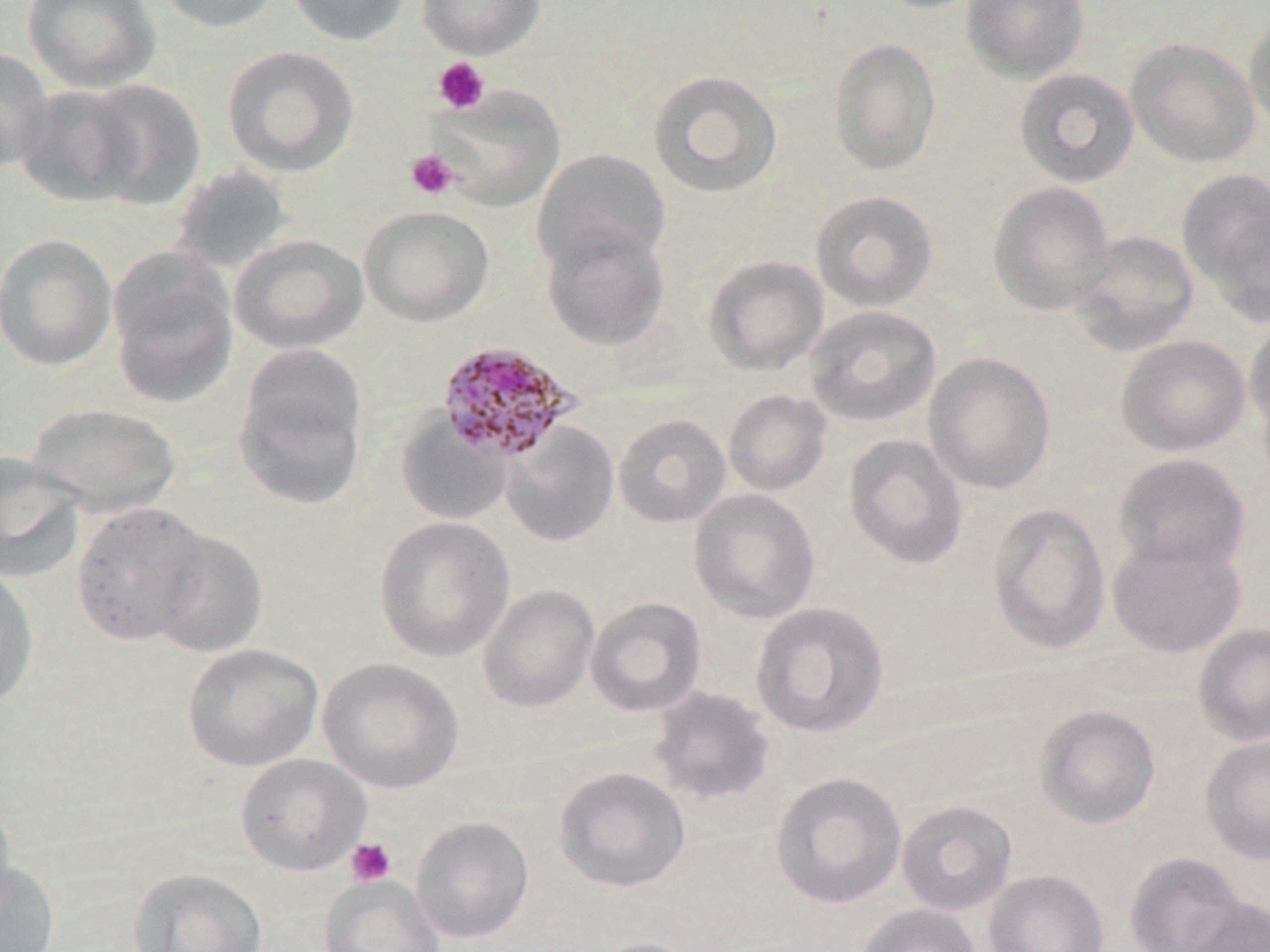

Approximate bounding boxes as (x1,y1)-(x2,y2) corner pairs in pixels. Platelet locations: (432,57)-(490,114), (405,149)-(458,200), (345,837)-(397,886). Plasmodium malariae-infected red blood cell locations: (435,341)-(579,463). Uninfected red blood cell locations: (22,0)-(161,93), (154,0)-(284,34), (286,0)-(410,46), (417,0)-(546,58), (871,0)-(984,14), (962,0)-(1090,84), (1244,9)-(1270,136), (828,37)-(941,176), (1125,37)-(1261,169), (222,45)-(359,176), (0,48)-(55,171), (1014,67)-(1140,187), (647,69)-(783,199), (81,79)-(206,210), (12,84)-(147,208), (429,84)-(566,212), (532,148)-(672,274), (168,164)-(293,276), (1177,168)-(1270,321), (987,181)-(1116,315), (810,190)-(939,312), (359,204)-(494,327), (540,222)-(671,350), (1068,231)-(1199,355), (0,233)-(117,371), (229,234)-(368,353), (106,247)-(240,410), (703,255)-(829,375), (804,305)-(942,427), (1244,315)-(1270,440), (1115,334)-(1251,457), (232,347)-(369,511), (924,351)-(1056,495), (723,389)-(831,496), (25,402)-(183,519), (394,412)-(514,526), (613,413)-(732,529), (501,420)-(620,547), (844,434)-(969,571), (0,452)-(87,584), (1113,452)-(1252,575), (688,488)-(821,624), (71,501)-(212,646), (986,502)-(1111,654), (374,516)-(515,662), (147,528)-(269,660), (1107,533)-(1246,658), (0,565)-(39,709), (477,585)-(600,713), (585,596)-(708,717), (750,601)-(890,739), (1193,623)-(1270,746), (181,643)-(325,772), (317,657)-(464,794), (649,686)-(777,808), (1035,704)-(1161,829), (1199,734)-(1270,865), (235,754)-(371,876), (553,766)-(691,893), (770,771)-(907,909), (0,795)-(16,922), (897,800)-(1018,916), (410,815)-(535,944), (1124,852)-(1247,952), (0,858)-(61,952), (126,867)-(269,952), (983,869)-(1110,952), (318,874)-(445,952), (1181,895)-(1270,952), (856,904)-(980,952), (586,937)-(706,952). Slide-level diagnosis: Plasmodium malariae. One field of a larger specimen. Captured at 1000x magnification. May-Grünwald-Giemsa stain. Thin blood film. Image is 1270×952 pixels. Optical microscopy.